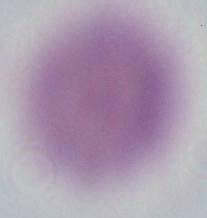
{
  "identification": "red blood cell",
  "modality": "micrograph",
  "magnification": "1000x"
}